Report the malaria status of this cell.
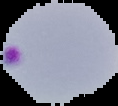

Parasitized.

preparation = thin blood film
image size = 118×106 pixels
image type = segmented cell region on a black background